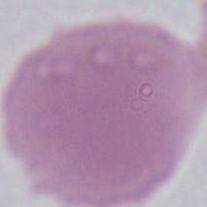
Captured at 1000x magnification. An erythrocyte is seen. Micrograph.